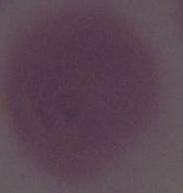
Summary:
  - Identification: red blood cell
  - Magnification: 1000x
  - Modality: micrograph